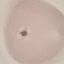
Summary:
  - Malaria status: uninfected
  - Capture: smartphone through the microscope eyepiece
  - Image type: automatically extracted cell patch, resized to 64 × 64 pixels
  - Stain: Giemsa
  - Preparation: thin blood film